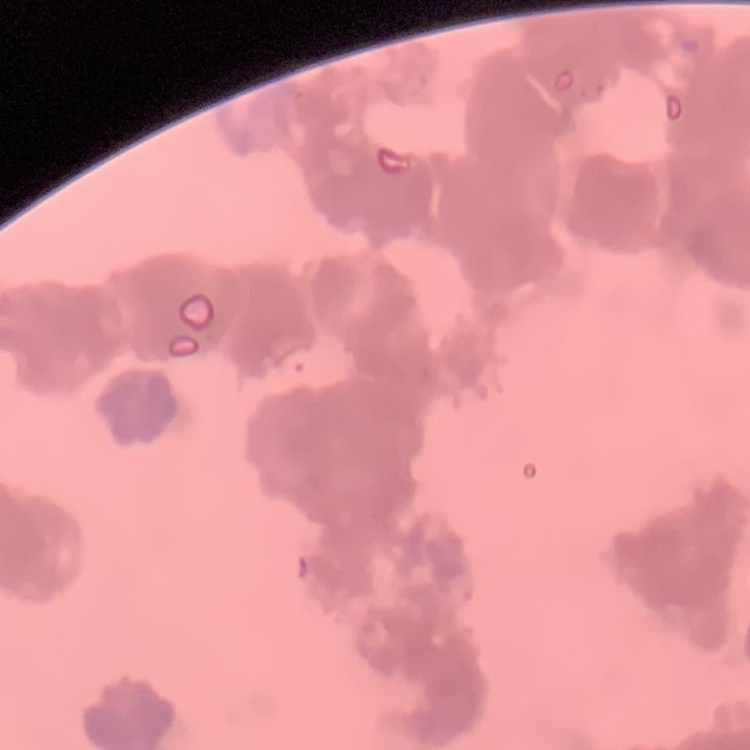

Summary:
  - Erythrocyte morphology: rouleaux formation
  - Stain: Field's or Giemsa
  - Preparation: thin blood film
  - Image type: square crop of a larger photomicrograph